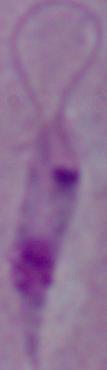
modality = micrograph
magnification = 1000x
identification = Leishmania